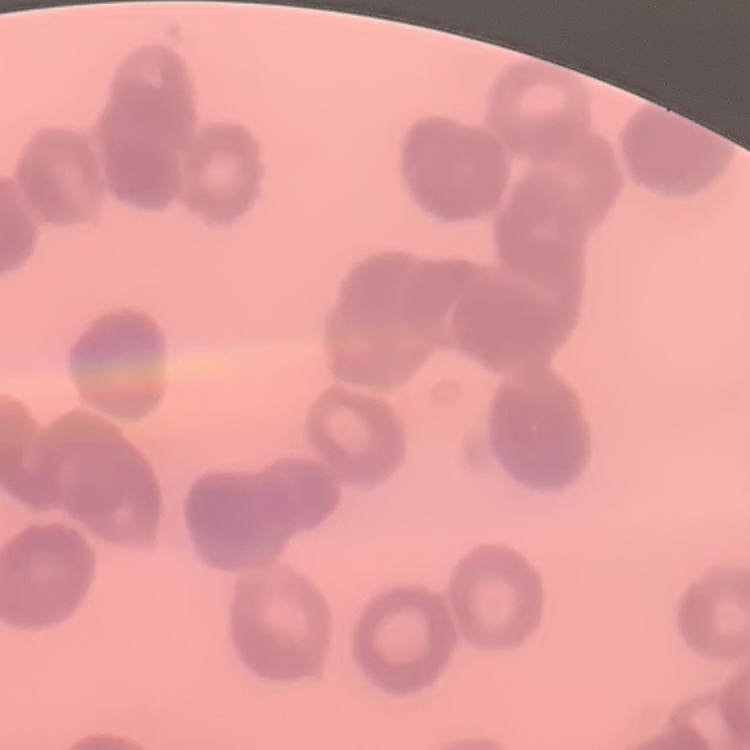 The red blood cells exhibit rouleaux formation. Thin peripheral smear. Square crop of a larger photomicrograph. Field's or Giemsa stain.